Locate every blood parasite and identify its species.
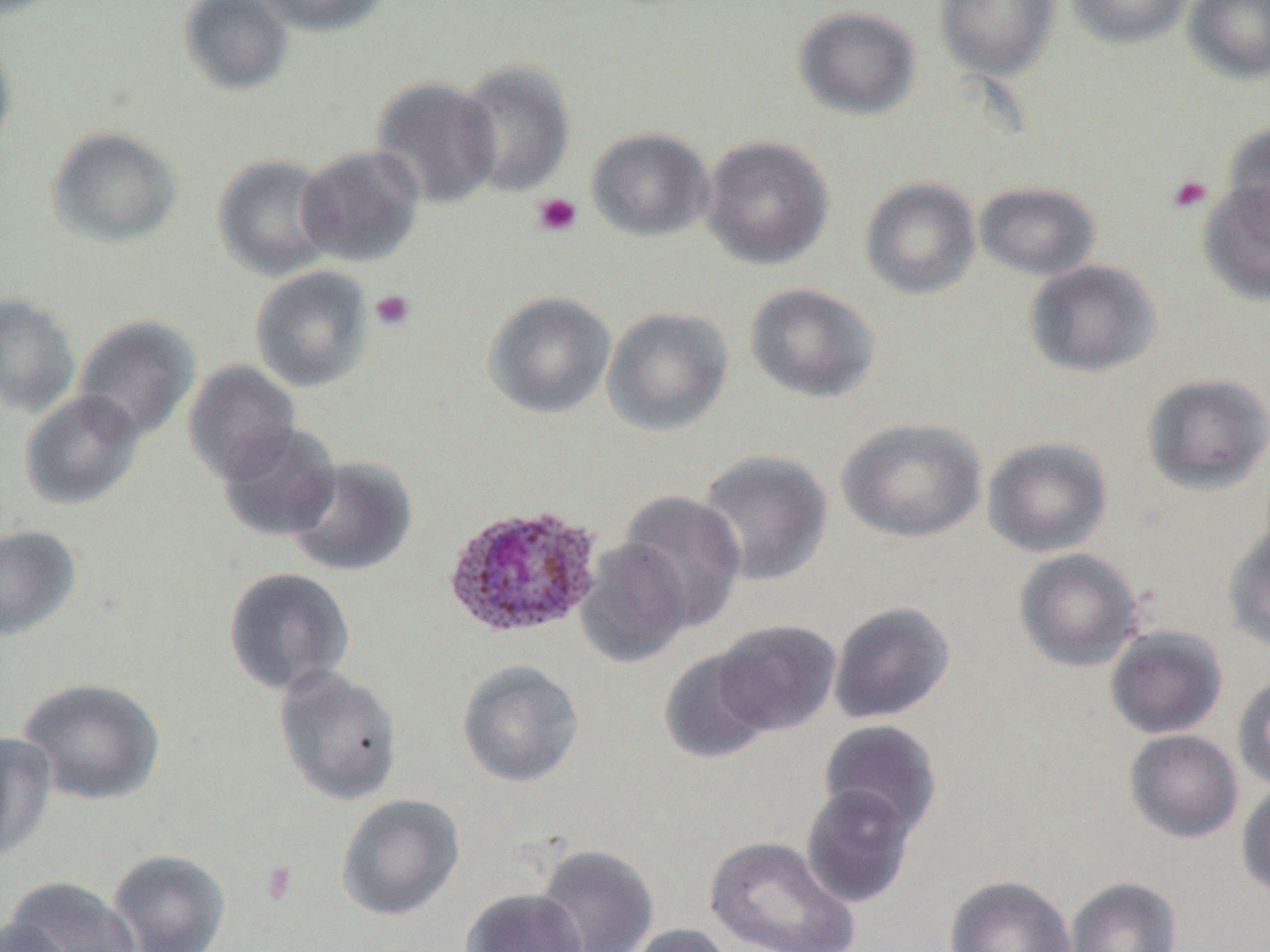

Approximate bounding boxes as (x1, y1, x2, y2) in pixels.
Plasmodium ovale-infected red blood cells: (441, 503, 605, 641).
No Plasmodium falciparum, Plasmodium malariae, Plasmodium vivax, Babesia divergens, or Trypanosoma brucei observed.

slide-level diagnosis = Plasmodium ovale
image size = 1270×952 pixels
platelet locations = approximate bounding boxes as (x1, y1, x2, y2) in pixels: (1167, 174, 1213, 214), (531, 192, 582, 237), (370, 289, 416, 331), (261, 863, 297, 905)
field of view = one of a larger specimen
uninfected red blood cell locations = approximate bounding boxes as (x1, y1, x2, y2) in pixels: (179, 0, 294, 95), (249, 0, 391, 36), (935, 0, 1060, 81), (1066, 0, 1195, 48), (1184, 0, 1270, 83), (792, 6, 922, 121), (0, 32, 17, 167), (456, 58, 576, 198), (370, 76, 503, 210), (1222, 122, 1270, 237), (45, 125, 183, 248), (586, 126, 714, 242), (700, 136, 834, 270), (296, 144, 425, 267), (212, 153, 338, 281), (859, 176, 981, 300), (975, 180, 1100, 280), (1197, 180, 1270, 305), (1023, 259, 1161, 377), (250, 265, 374, 392), (744, 283, 880, 403), (482, 290, 616, 418), (0, 292, 82, 419), (601, 305, 734, 437), (73, 313, 202, 441), (182, 360, 300, 484), (1141, 372, 1270, 496), (19, 390, 146, 510), (837, 417, 986, 543), (218, 421, 342, 541), (982, 436, 1113, 558), (695, 449, 833, 586), (284, 456, 418, 578), (617, 489, 746, 633), (1222, 521, 1270, 652), (0, 524, 82, 641), (575, 539, 691, 668), (1013, 548, 1143, 672), (223, 566, 355, 696), (829, 601, 956, 725), (713, 619, 841, 736), (1105, 625, 1228, 739), (658, 648, 775, 764), (457, 659, 584, 788), (272, 664, 403, 806), (1232, 672, 1270, 792), (17, 677, 166, 806), (818, 720, 941, 838), (1124, 729, 1244, 843), (0, 731, 57, 863), (1237, 781, 1270, 898), (801, 784, 917, 908), (335, 794, 465, 921), (705, 835, 860, 952), (535, 844, 659, 952), (108, 848, 232, 952), (945, 875, 1076, 952), (3, 876, 143, 952), (1066, 877, 1182, 952), (460, 888, 586, 952), (0, 918, 70, 952), (621, 923, 736, 952)
modality = light microscopy
magnification = 1000x
preparation = thin blood film